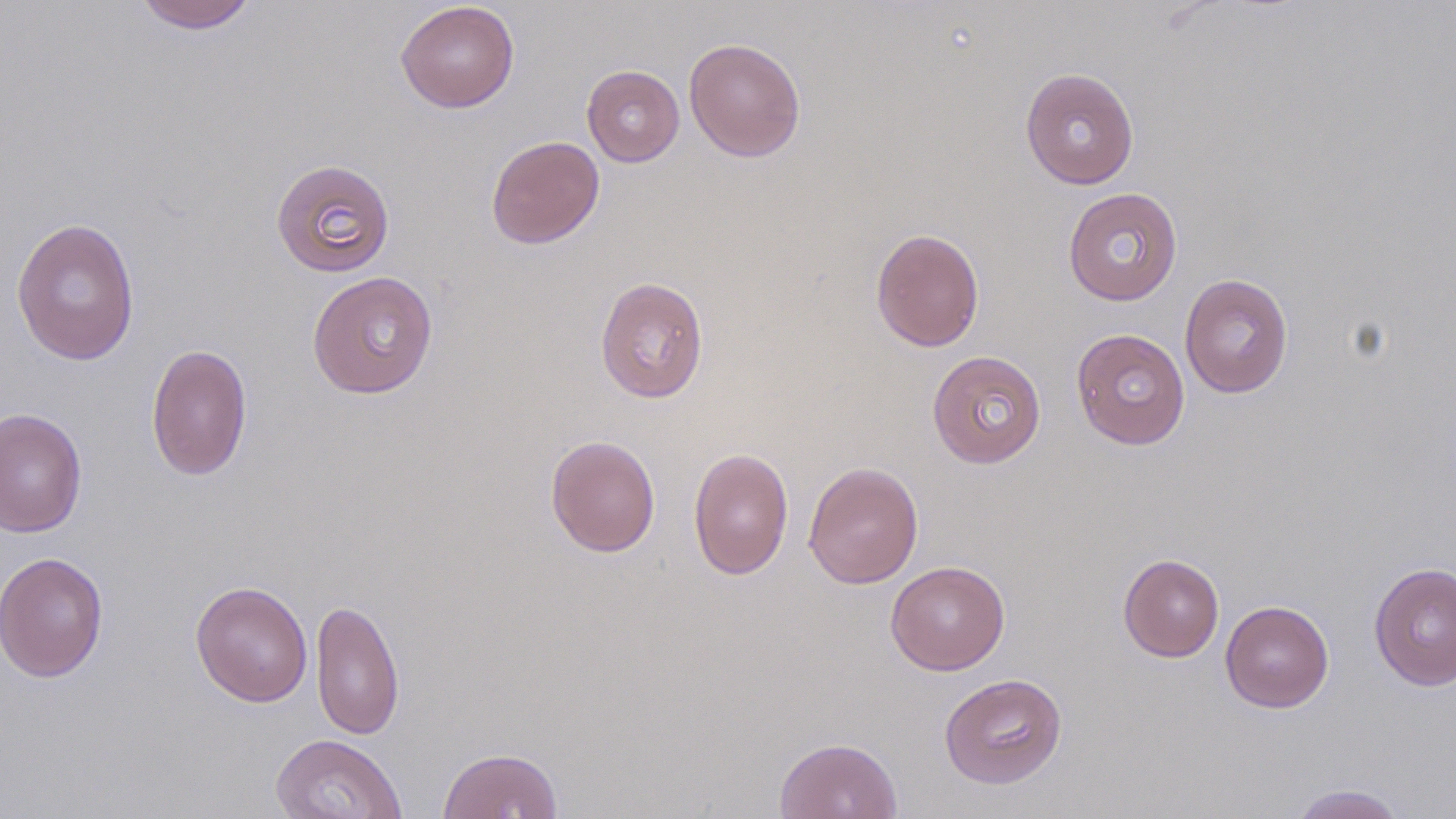
Summary:
  - Coordinate format: approximate bounding boxes as (x1, y1, x2, y2) in pixels
  - Uninfected red blood cell locations: (133, 1, 259, 33), (395, 1, 520, 113), (684, 37, 806, 162), (582, 65, 684, 166), (1020, 67, 1140, 189), (486, 135, 604, 249), (271, 158, 395, 278), (1063, 187, 1183, 305), (11, 217, 141, 365), (870, 227, 985, 352), (306, 270, 438, 399), (1179, 273, 1294, 399), (595, 276, 709, 404), (1071, 328, 1190, 450), (145, 343, 253, 481), (927, 350, 1046, 468), (0, 407, 88, 538), (545, 434, 661, 557), (688, 446, 794, 580), (803, 461, 924, 589), (0, 551, 109, 682), (1118, 553, 1224, 662), (886, 560, 1010, 676), (1369, 560, 1456, 691), (190, 580, 314, 707), (310, 599, 405, 739), (1220, 600, 1334, 713), (939, 672, 1068, 789), (270, 733, 408, 819), (774, 736, 903, 819), (437, 746, 563, 819), (1288, 784, 1408, 818)
  - Slide-level diagnosis: no evidence of blood parasites
  - Field of view: single
  - Image size: 1456×819 pixels
  - Magnification: 1000x
  - Modality: light microscopy
  - Preparation: thin blood film
  - Stain: May-Grünwald-Giemsa